Report the malaria status of this cell.
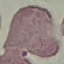

It is uninfected.

Summary:
  - Preparation: thin smear
  - Image type: automatically extracted cell patch, resized to 64 × 64 pixels
  - Stain: Giemsa
  - Capture: smartphone through the microscope eyepiece